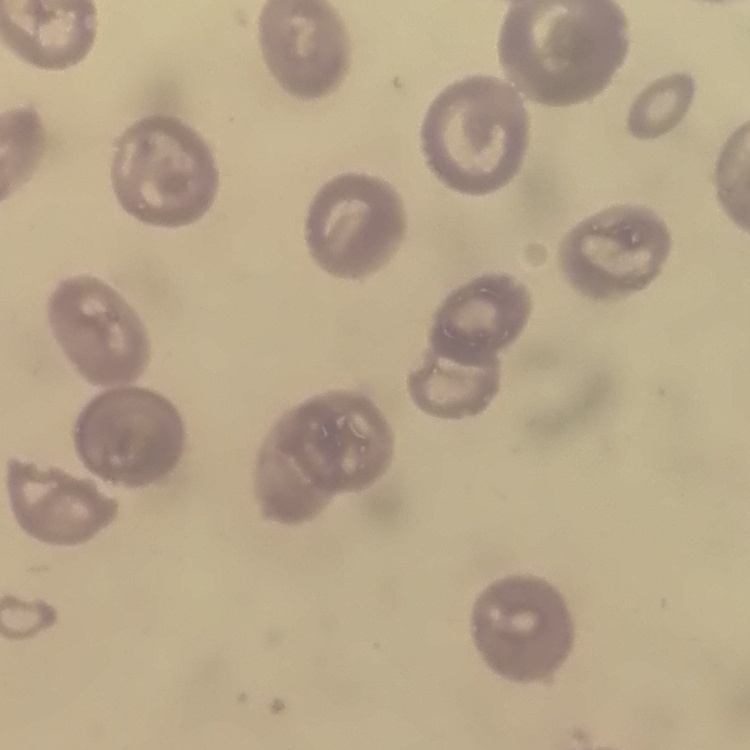

The erythrocytes show no rouleaux formation. Square crop of a larger photomicrograph. Field's or Giemsa stain. Thin blood smear.